Identify the cell.
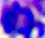

This is a leukocyte.

Micrograph. 400x magnification.